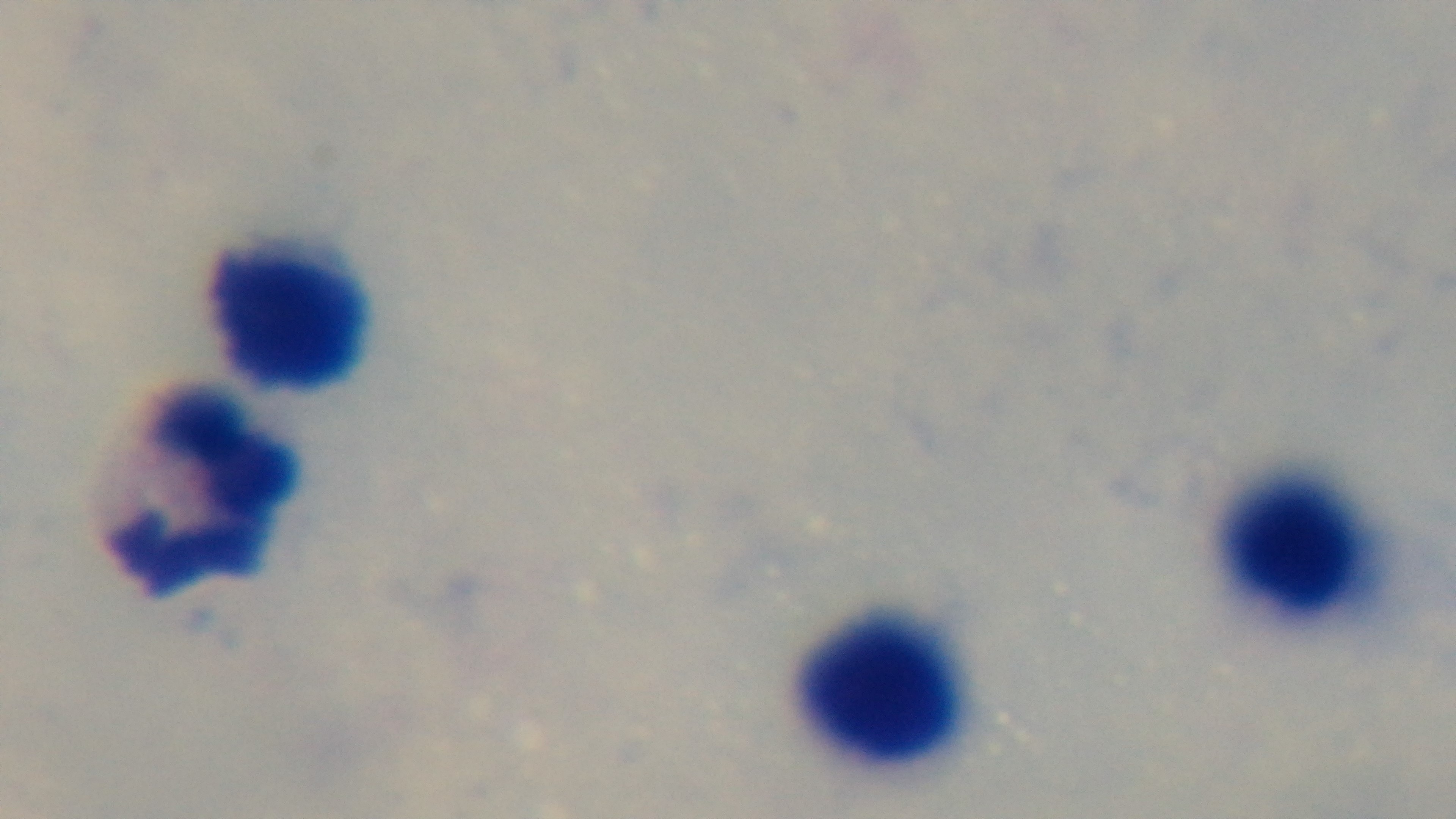
malaria status = uninfected
preparation = thick
stain = Giemsa
field of view = one from the slide
objective = 100x oil immersion
modality = light microscopy
capture = mounted 4K digital camera